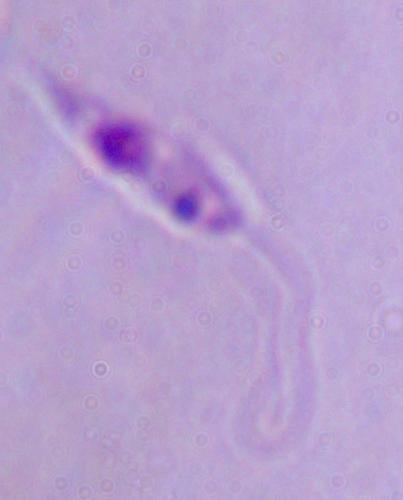

identification = Leishmania
magnification = 1000x
modality = micrograph